Assess this cell for malaria.
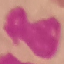
Uninfected.

Summary:
  - Capture: smartphone camera at the microscope eyepiece
  - Image type: automatically extracted cell patch, resized to 64 × 64 pixels
  - Preparation: thin smear
  - Stain: Giemsa